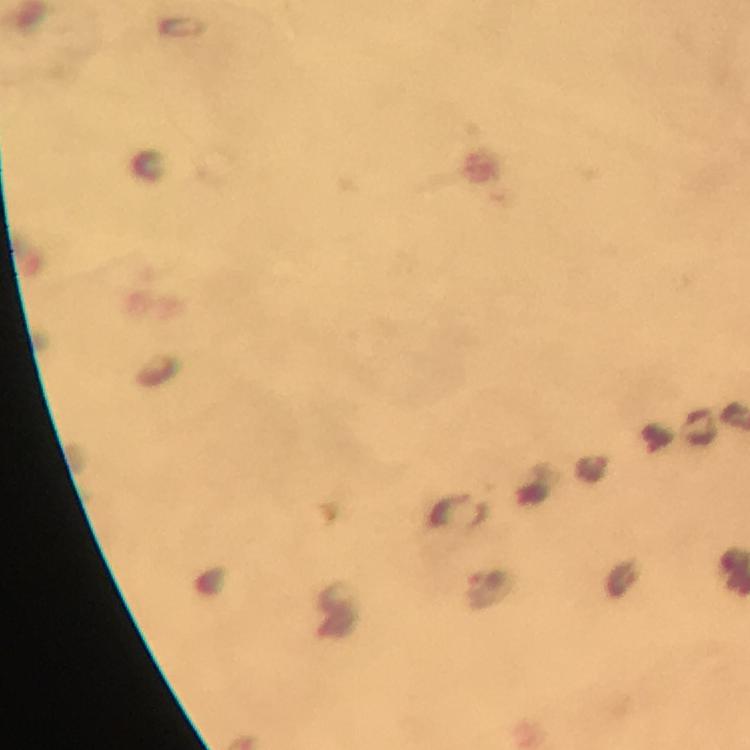
Approximate centers as {x, y} in pixels.
Summary:
  - Plasmodium parasite locations: {487, 579}
  - Stain: Giemsa
  - Preparation: thick smear
  - Immersion oil: applied
  - Context: from a malaria diagnostic workup
  - Cropped from: one field of view
  - Image size: 750×750 pixels
  - Magnification: 100x
  - Capture: smartphone photograph through a microscope